Give the position of every malaria parasite.
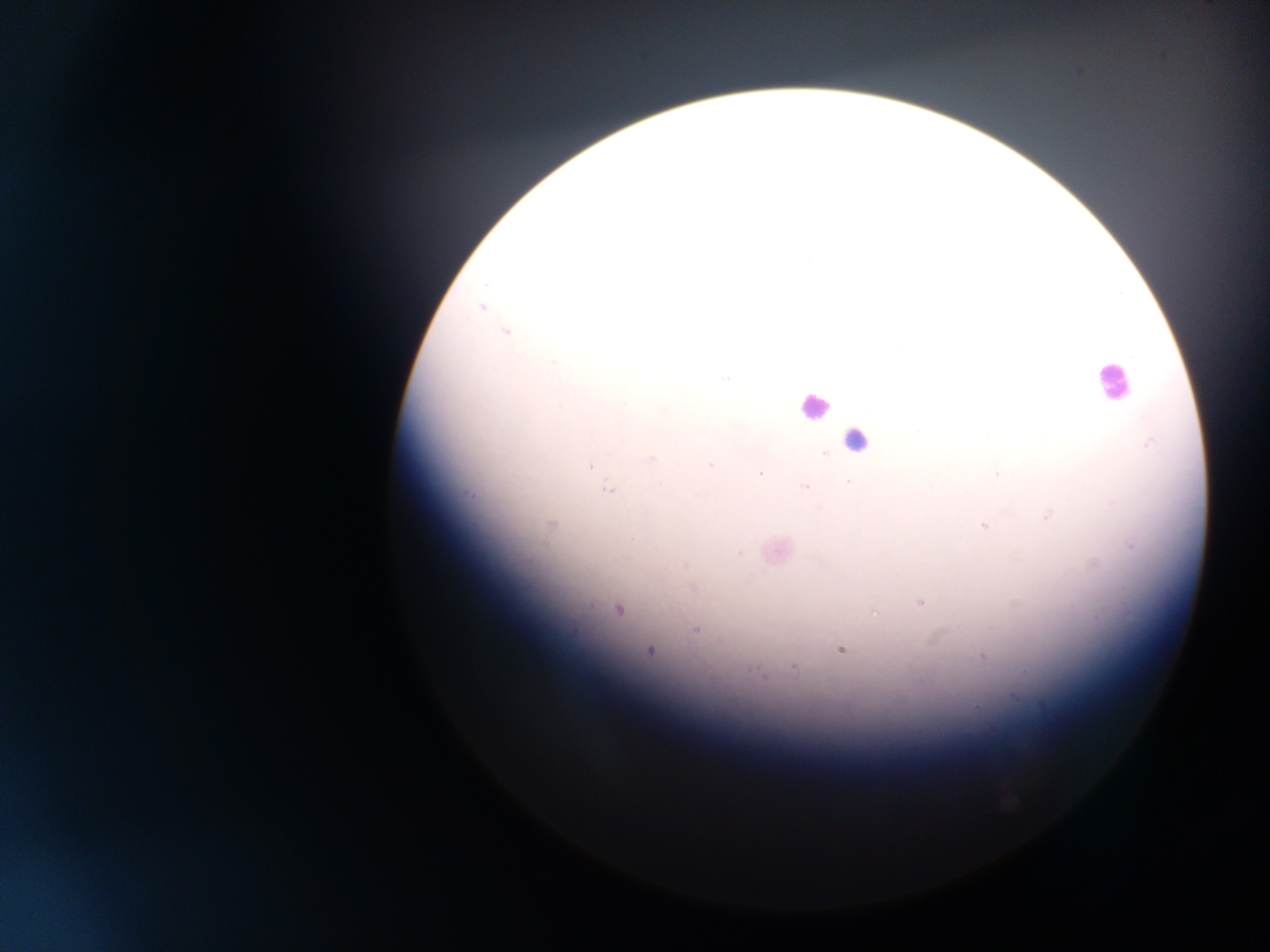
Approximate centers as (x, y) in pixels.
Malaria parasites: (481, 307), (505, 333), (554, 363), (726, 379), (664, 410), (917, 431), (1148, 445), (824, 453), (650, 459), (711, 465), (591, 466), (760, 474), (997, 474), (848, 482), (806, 487), (608, 491), (468, 494), (1047, 517), (550, 524), (983, 525), (1131, 545), (740, 554), (920, 603), (618, 610), (873, 612), (695, 629), (840, 650), (649, 651), (983, 657), (793, 667), (753, 670), (759, 673), (1042, 705), (976, 707).

Summary:
  - Leukocyte locations: (1111, 382), (813, 407), (856, 440)
  - Capture: mobile-phone photograph through a microscope
  - Country: Ghana
  - Preparation: thick blood smear
  - Image size: 1270×952 pixels
  - Field of view: single